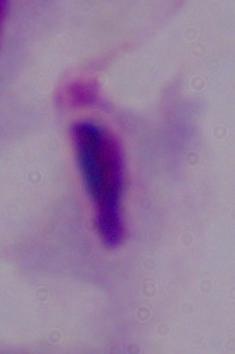
magnification = 1000x
identification = trichomonad
modality = photomicrograph